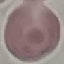 Result: no malaria parasites detected. Photographed with a smartphone camera at the microscope eyepiece. Thin blood film. Giemsa-stained preparation. Automatically extracted cell patch, resized to 64 × 64 pixels.